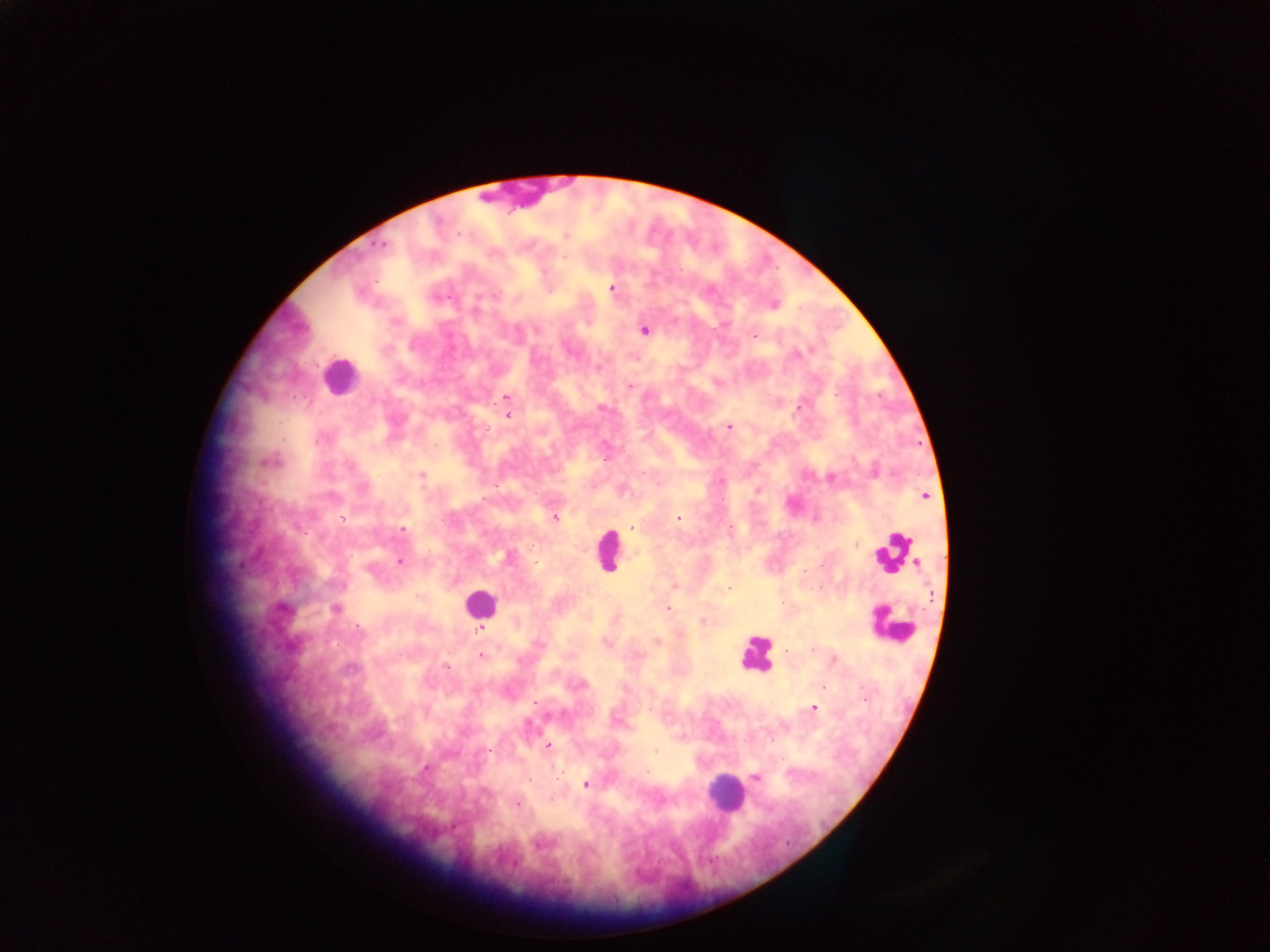 Approximate centers as [x, y] in pixels. Plasmodium parasite locations: [565, 236], [381, 244], [564, 256], [611, 288], [495, 296], [772, 304], [645, 330], [755, 336], [598, 367], [629, 386], [507, 398], [601, 407], [798, 407], [507, 415], [729, 426], [269, 462], [873, 471], [422, 476], [830, 478], [621, 490], [925, 495], [554, 517], [676, 519], [632, 528], [402, 529], [730, 529], [507, 557], [400, 561], [674, 586], [727, 589], [667, 607], [336, 608], [703, 620], [481, 630], [657, 641], [606, 643], [540, 645], [480, 655], [821, 687], [813, 708], [547, 746], [656, 750], [755, 777], [586, 784], [516, 804]. Leukocyte locations: [339, 375], [607, 550], [894, 552], [478, 603], [892, 624], [755, 653], [725, 792]. Collected in Ghana. Thick blood smear. Single field of view. Image is 1270×952 pixels. Mobile-phone photograph taken through the microscope.